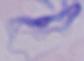
Summary:
  - Identification: trypanosome
  - Magnification: 1000x
  - Modality: photomicrograph